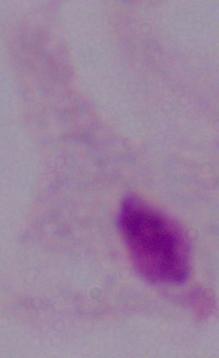

{
  "magnification": "1000x",
  "modality": "micrograph",
  "identification": "trichomonad"
}